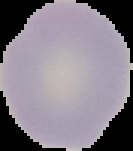

Summary:
  - Preparation: thin blood film
  - Image size: 133×151 pixels
  - Image type: segmented cell region on a black background
  - Result: negative for Plasmodium parasites